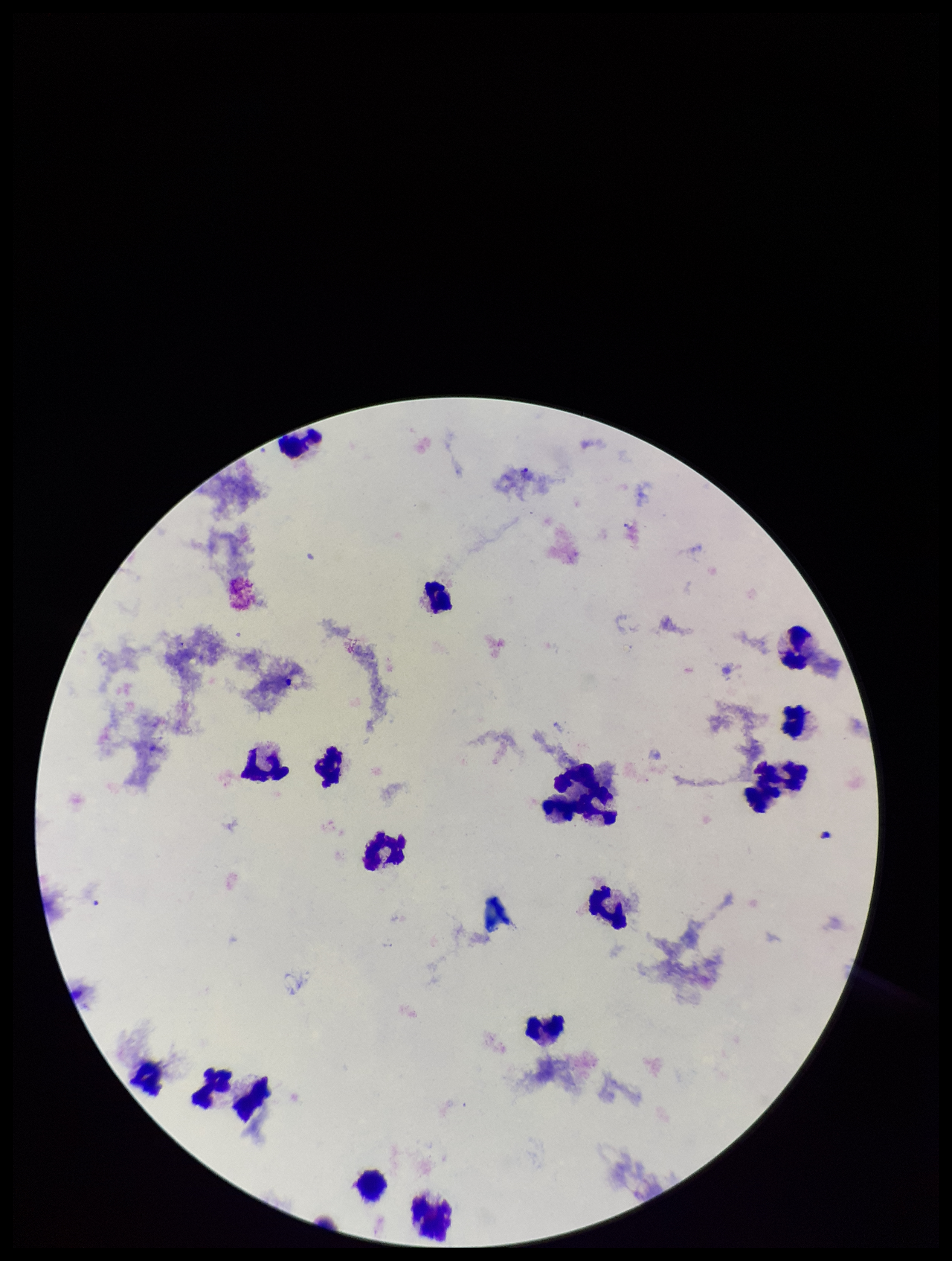
stain = Giemsa
parasite count = 0
image size = 952×1261 pixels
Plasmodium parasites = none seen
capture = smartphone photograph through the microscope eyepiece
patient malaria status = negative
leukocyte count = 15
field of view = single
preparation = thick blood smear